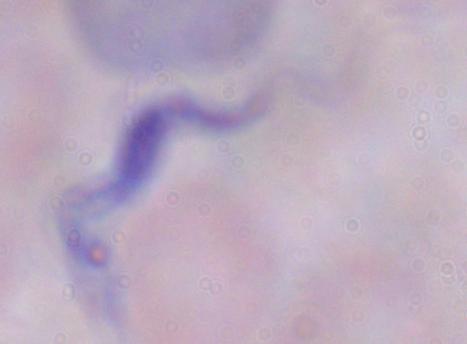 A trypanosome is seen. Photomicrograph. Captured at 1000x magnification.